Classify this cell by malaria status.
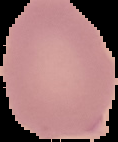
It is uninfected.

preparation: thin blood film
image_type: segmented cell region with the area outside set to black
image_size: 118×142 pixels